Identify the parasite.
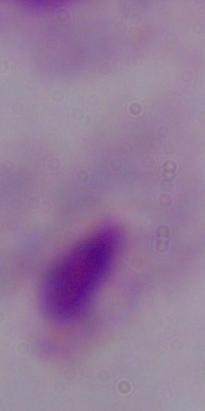

A trichomonad.

Summary:
  - Modality: photomicrograph
  - Magnification: 1000x